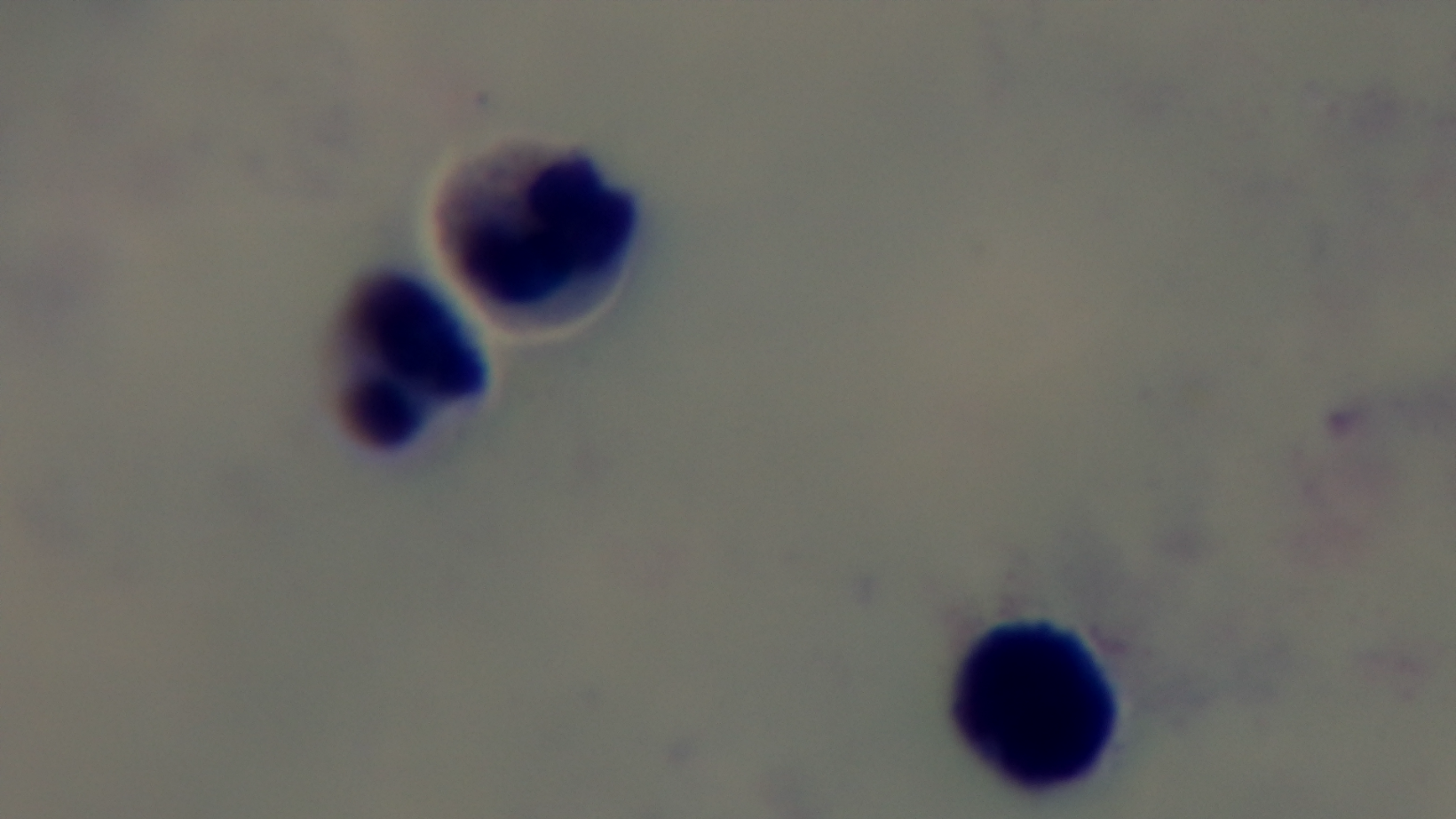

capture: mounted 4K digital camera
preparation: thick smear
field_of_view: single
malaria_status: uninfected
objective: 100x oil immersion
stain: Giemsa
modality: light microscopy